Locate and identify every blood parasite.
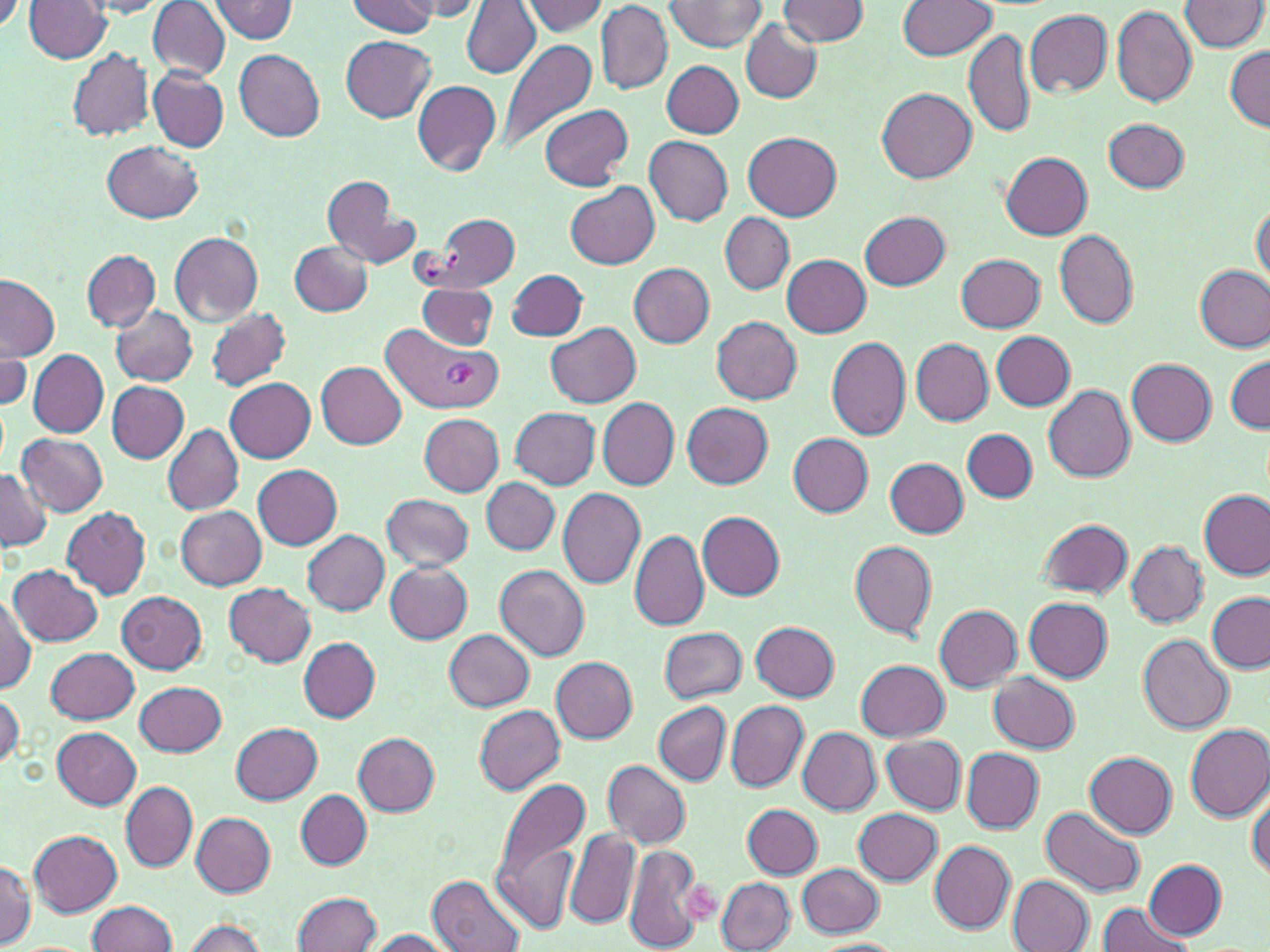

Approximate bounding boxes as (x1, y1, x2, y2) in pixels.
Plasmodium vivax-infected red blood cells: (386, 327, 505, 415).
No Plasmodium falciparum, Plasmodium ovale, Plasmodium malariae, Babesia divergens, or Trypanosoma brucei observed.

Summary:
  - Uninfected red blood cell locations: (0, 0, 24, 34), (210, 0, 298, 41), (347, 0, 438, 38), (397, 0, 486, 19), (522, 0, 609, 36), (667, 0, 767, 52), (778, 0, 869, 45), (898, 0, 996, 59), (1181, 0, 1269, 52), (24, 1, 113, 63), (86, 2, 174, 19), (149, 2, 230, 80), (463, 2, 540, 78), (596, 2, 672, 95), (752, 2, 852, 75), (1111, 5, 1198, 108), (1024, 9, 1113, 97), (742, 20, 821, 104), (965, 28, 1035, 139), (341, 35, 437, 121), (497, 38, 598, 156), (1226, 44, 1269, 131), (68, 49, 154, 142), (234, 50, 325, 141), (662, 61, 744, 137), (149, 67, 228, 152), (412, 80, 500, 175), (877, 87, 976, 183), (538, 103, 634, 191), (1103, 118, 1191, 194), (744, 132, 841, 221), (645, 135, 733, 226), (102, 141, 203, 223), (1002, 152, 1094, 241), (322, 176, 416, 271), (566, 183, 660, 269), (1251, 202, 1269, 291), (859, 210, 950, 289), (721, 213, 794, 294), (433, 214, 518, 290), (1054, 230, 1139, 329), (169, 231, 264, 326), (289, 241, 372, 314), (83, 250, 160, 330), (781, 254, 872, 338), (957, 254, 1047, 332), (628, 263, 715, 347), (1194, 264, 1269, 353), (506, 269, 588, 341), (0, 274, 59, 361), (416, 281, 498, 350), (109, 305, 197, 386), (205, 306, 291, 391), (712, 316, 802, 404), (546, 321, 641, 407), (991, 331, 1075, 411), (826, 336, 911, 441), (0, 337, 31, 416), (911, 338, 993, 425), (28, 349, 109, 436), (1226, 355, 1269, 432), (1126, 358, 1216, 448), (316, 361, 408, 448), (224, 377, 316, 462), (107, 381, 190, 463), (1044, 384, 1135, 483), (598, 397, 679, 488), (682, 403, 773, 488), (510, 407, 600, 490), (420, 413, 504, 496), (162, 423, 244, 515), (962, 429, 1037, 503), (17, 432, 109, 516), (787, 433, 873, 516), (884, 457, 969, 538), (252, 464, 342, 549), (0, 469, 51, 551), (481, 478, 561, 554), (557, 488, 645, 589), (1199, 490, 1268, 579), (381, 494, 474, 572), (60, 505, 150, 599), (174, 505, 267, 589), (697, 511, 786, 599), (1036, 518, 1133, 599), (629, 529, 711, 631), (303, 530, 389, 615), (849, 540, 938, 640), (1125, 540, 1207, 627), (385, 561, 473, 644), (496, 564, 591, 660), (9, 565, 103, 648), (224, 582, 316, 667), (117, 590, 208, 672), (1207, 593, 1269, 672), (0, 594, 37, 695), (1024, 597, 1112, 683), (933, 603, 1022, 692), (750, 621, 840, 702), (659, 627, 748, 703), (443, 629, 533, 712), (1139, 634, 1233, 736), (297, 637, 380, 722), (46, 647, 139, 725), (550, 657, 637, 742), (855, 660, 949, 740), (989, 672, 1079, 753), (135, 681, 227, 755), (1, 692, 23, 772), (725, 700, 808, 791), (653, 701, 730, 785), (473, 703, 566, 795), (230, 722, 323, 804), (1185, 724, 1270, 820), (53, 727, 141, 809), (796, 727, 881, 815), (354, 733, 438, 815), (881, 734, 966, 815), (962, 748, 1044, 831), (1085, 752, 1178, 837), (603, 760, 689, 847), (491, 774, 593, 921), (121, 782, 197, 872), (296, 790, 371, 870), (1247, 790, 1269, 882), (742, 804, 822, 878), (1042, 806, 1145, 896), (853, 807, 942, 887), (191, 811, 275, 896), (29, 829, 122, 916), (564, 830, 640, 928), (930, 841, 1016, 932), (623, 842, 705, 952), (0, 858, 36, 945), (1144, 859, 1225, 938), (797, 863, 883, 937), (1007, 874, 1095, 951), (430, 875, 526, 952), (717, 878, 796, 952), (293, 892, 382, 952), (87, 899, 179, 951), (1096, 902, 1194, 951), (179, 918, 271, 952), (358, 928, 457, 951), (810, 939, 907, 951)
  - Platelet locations: (680, 880, 724, 923)
  - Slide-level diagnosis: Plasmodium vivax
  - Field of view: one of a larger specimen
  - Modality: optical microscopy
  - Stain: May-Grünwald-Giemsa
  - Image size: 1270×952 pixels
  - Magnification: 1000x
  - Preparation: thin blood film